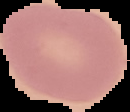

{
  "image_size": "130×112 pixels",
  "malaria_status": "uninfected",
  "image_type": "segmented cell region with the area outside set to black",
  "preparation": "thin blood smear"
}